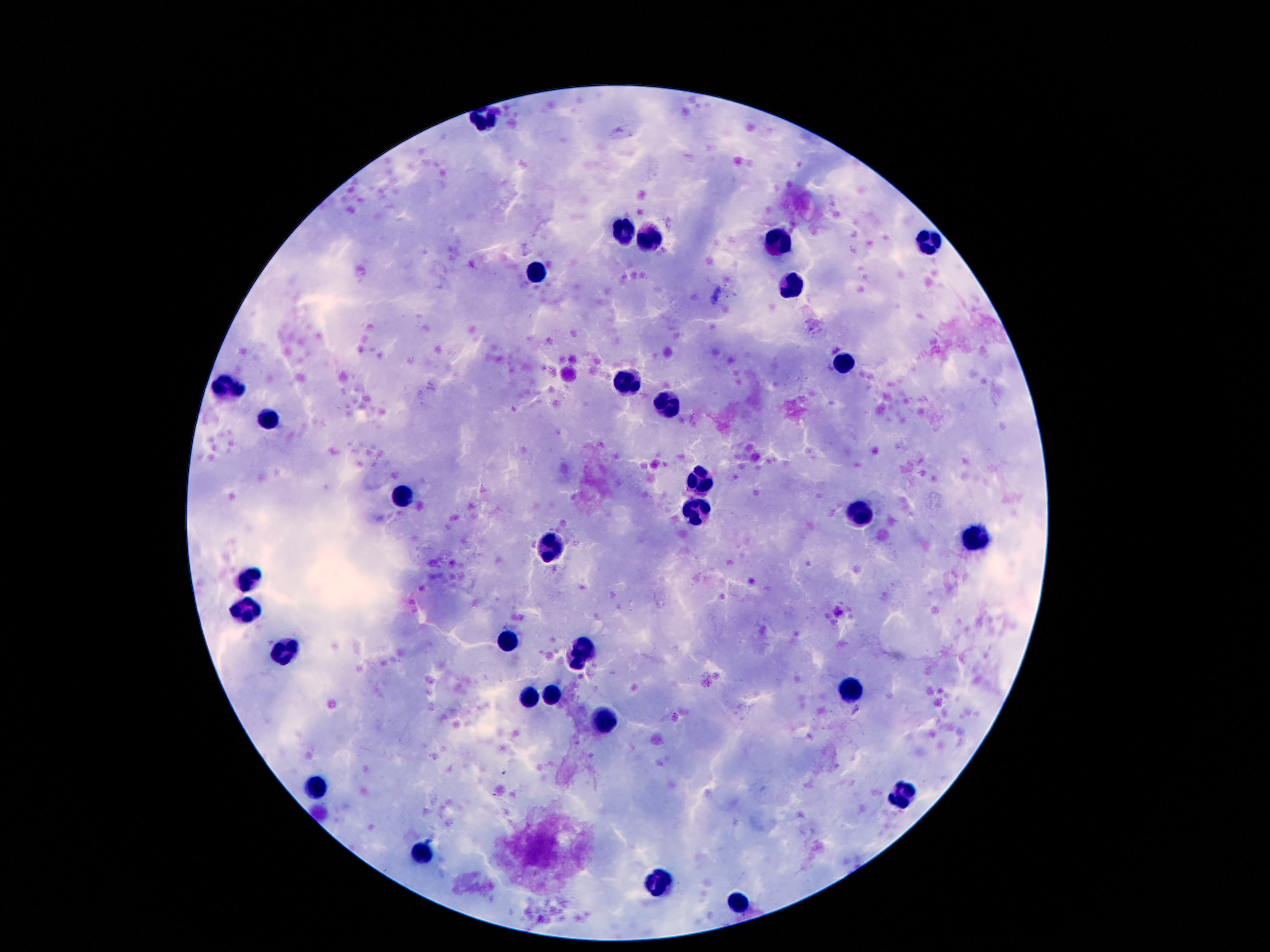
Approximate centers as {x, y} in pixels.
Summary:
  - Leukocyte locations: {483, 119}, {625, 233}, {781, 235}, {650, 236}, {930, 239}, {536, 274}, {794, 284}, {842, 363}, {628, 382}, {228, 385}, {669, 402}, {267, 420}, {699, 479}, {402, 499}, {694, 513}, {860, 514}, {979, 538}, {552, 547}, {249, 577}, {247, 607}, {509, 643}, {585, 644}, {281, 651}, {576, 663}, {852, 688}, {530, 696}, {551, 696}, {603, 721}, {316, 787}, {900, 796}, {421, 856}, {658, 882}, {738, 902}
  - Stain: Giemsa
  - Magnification: 100x
  - Preparation: thick peripheral-blood smear
  - Field of view: single
  - Image size: 1270×952 pixels
  - Capture: smartphone camera through the microscope eyepiece
  - Patient malaria status: not infected